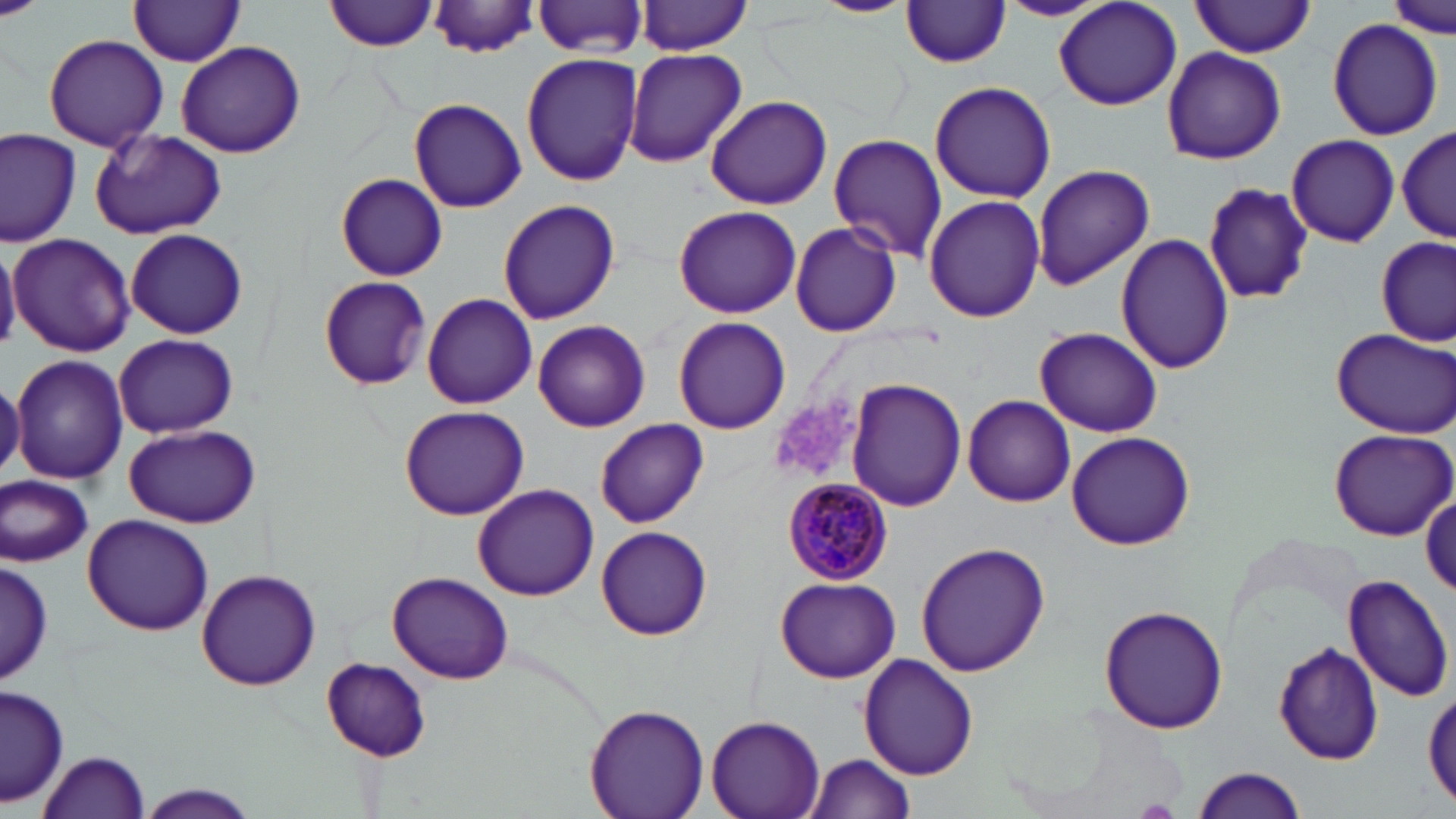
Approximate bounding boxes as (x1, y1, x2, y2) in pixels. Plasmodium malariae-infected red blood cell locations: (782, 476, 895, 587). Uninfected red blood cell locations: (326, 0, 437, 51), (811, 0, 916, 17), (997, 0, 1113, 21), (1388, 0, 1452, 37), (429, 1, 542, 57), (534, 1, 649, 57), (638, 1, 755, 54), (899, 1, 1013, 68), (126, 2, 248, 65), (1191, 2, 1316, 56), (1054, 3, 1183, 110), (1325, 18, 1445, 139), (43, 35, 169, 150), (176, 40, 305, 158), (1161, 47, 1286, 164), (623, 48, 745, 167), (522, 52, 643, 186), (928, 80, 1057, 204), (705, 96, 832, 210), (409, 98, 526, 212), (1397, 125, 1453, 243), (89, 129, 225, 240), (0, 130, 80, 245), (827, 132, 947, 261), (1286, 134, 1398, 247), (1031, 163, 1155, 293), (335, 173, 447, 282), (1206, 182, 1315, 306), (924, 195, 1046, 323), (496, 199, 620, 324), (672, 205, 802, 317), (789, 222, 903, 338), (125, 228, 247, 339), (8, 233, 136, 355), (1116, 234, 1234, 375), (1377, 237, 1453, 346), (0, 241, 20, 353), (318, 275, 431, 389), (422, 292, 538, 410), (672, 316, 791, 435), (532, 319, 650, 433), (1329, 325, 1456, 437), (1035, 328, 1163, 437), (114, 333, 238, 438), (11, 354, 127, 483), (848, 379, 967, 512), (961, 395, 1076, 506), (399, 404, 531, 520), (595, 418, 708, 527), (124, 423, 259, 529), (1327, 428, 1456, 539), (1065, 431, 1196, 550), (1, 474, 95, 567), (472, 484, 602, 601), (1421, 494, 1455, 601), (84, 515, 213, 636), (596, 526, 712, 640), (916, 540, 1050, 678), (0, 560, 53, 684), (195, 569, 323, 691), (388, 573, 512, 685), (1342, 573, 1452, 700), (774, 577, 902, 684), (1098, 604, 1227, 733), (1273, 642, 1385, 765), (858, 653, 980, 780), (321, 658, 431, 760), (1, 685, 68, 808), (1423, 689, 1455, 807), (585, 704, 709, 819), (707, 716, 823, 819), (37, 748, 152, 819), (803, 754, 917, 818), (1190, 766, 1308, 819), (133, 783, 260, 819). Platelet locations: (770, 391, 865, 482). Slide-level diagnosis: Plasmodium malariae. May-Grünwald-Giemsa-stained preparation. One field of a larger specimen. Light microscopy. Image is 1456×819 pixels. Thin blood smear. Captured at 1000x magnification.